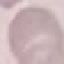
result = no malaria parasites seen
capture = smartphone through the microscope eyepiece
image type = automatically extracted cell patch, resized to 64 × 64 pixels
stain = Giemsa
preparation = thin blood film